Name the parasite shown.
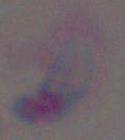

This is Toxoplasma gondii.

magnification = 1000x
modality = micrograph